Outline each blood parasite and name the species.
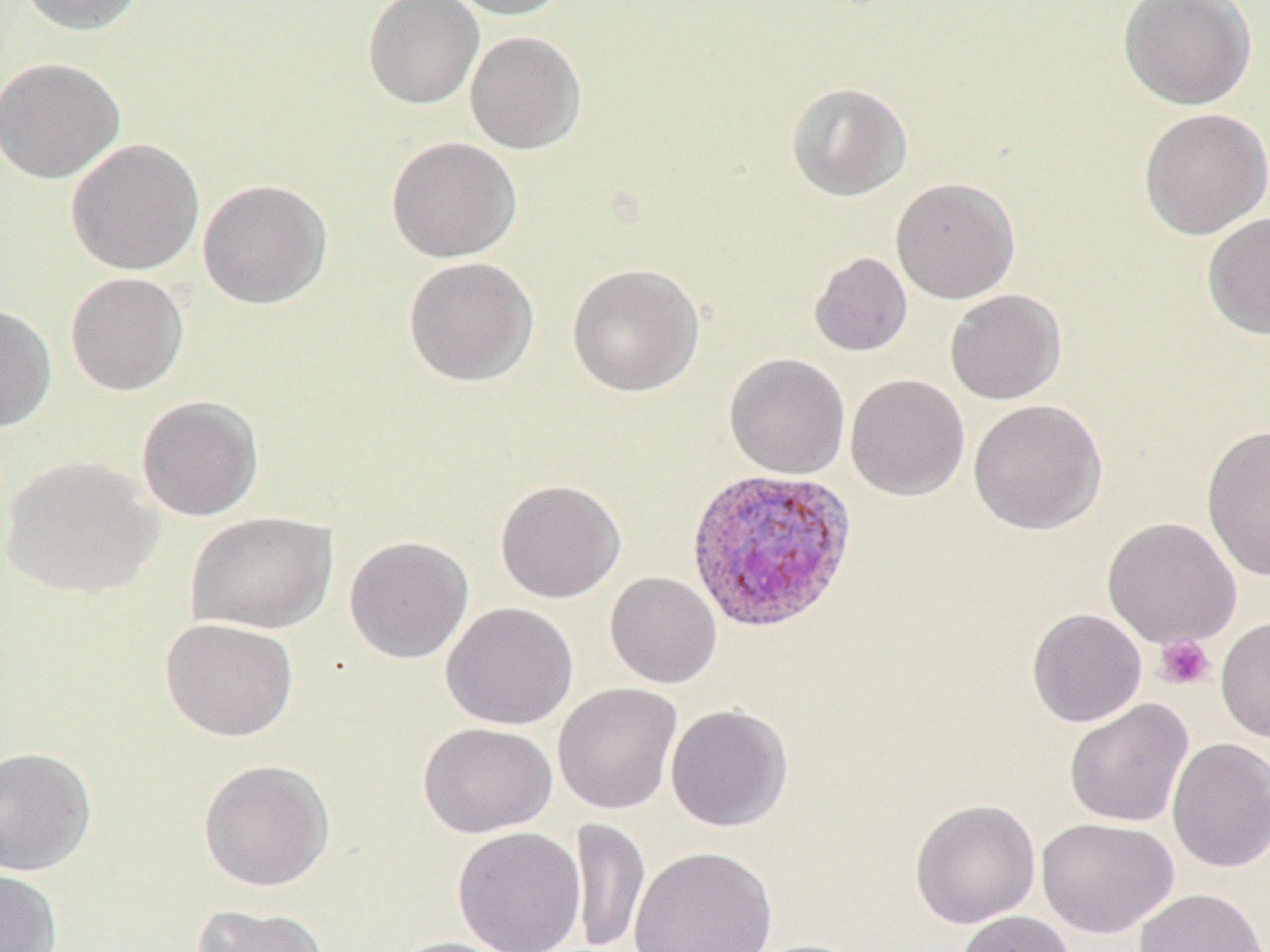
Approximate bounding boxes as [x1, y1, x2, y2] in pixels.
Plasmodium ovale-infected red blood cells: [684, 467, 858, 633].
No Plasmodium falciparum, Plasmodium malariae, Plasmodium vivax, Babesia divergens, or Trypanosoma brucei observed.

Uninfected red blood cell locations: [16, 0, 148, 37], [362, 0, 485, 110], [443, 0, 573, 20], [1118, 1, 1257, 110], [464, 30, 587, 155], [0, 56, 126, 185], [785, 81, 913, 203], [1138, 107, 1270, 240], [385, 135, 523, 263], [65, 137, 205, 276], [891, 176, 1021, 304], [197, 178, 333, 310], [1202, 211, 1270, 340], [809, 251, 913, 357], [402, 256, 540, 387], [566, 263, 705, 397], [65, 272, 189, 397], [944, 288, 1067, 405], [0, 302, 58, 434], [724, 353, 851, 479], [844, 373, 970, 501], [135, 395, 265, 522], [967, 398, 1108, 536], [1201, 423, 1270, 581], [1, 454, 164, 601], [494, 478, 626, 603], [184, 511, 338, 635], [1102, 516, 1242, 649], [343, 535, 475, 663], [605, 571, 723, 688], [440, 602, 579, 730], [1026, 608, 1148, 727], [1215, 614, 1270, 743], [159, 617, 299, 742], [552, 682, 683, 816], [1064, 698, 1193, 828], [665, 703, 793, 832], [417, 722, 557, 838], [1167, 737, 1270, 874], [0, 746, 97, 877], [197, 759, 335, 892], [909, 798, 1041, 929], [1036, 816, 1179, 938], [568, 817, 650, 952], [452, 826, 587, 952], [629, 846, 778, 952], [0, 868, 63, 952], [1135, 888, 1268, 952], [190, 902, 333, 952], [954, 910, 1076, 952], [383, 936, 522, 952], [740, 938, 871, 952]. Platelet locations: [1153, 633, 1215, 691]. Slide-level diagnosis: Plasmodium ovale. Single field of view. May-Grünwald-Giemsa stain. Light microscopy. Image is 1270×952 pixels. Thin blood smear. Captured at 1000x magnification.